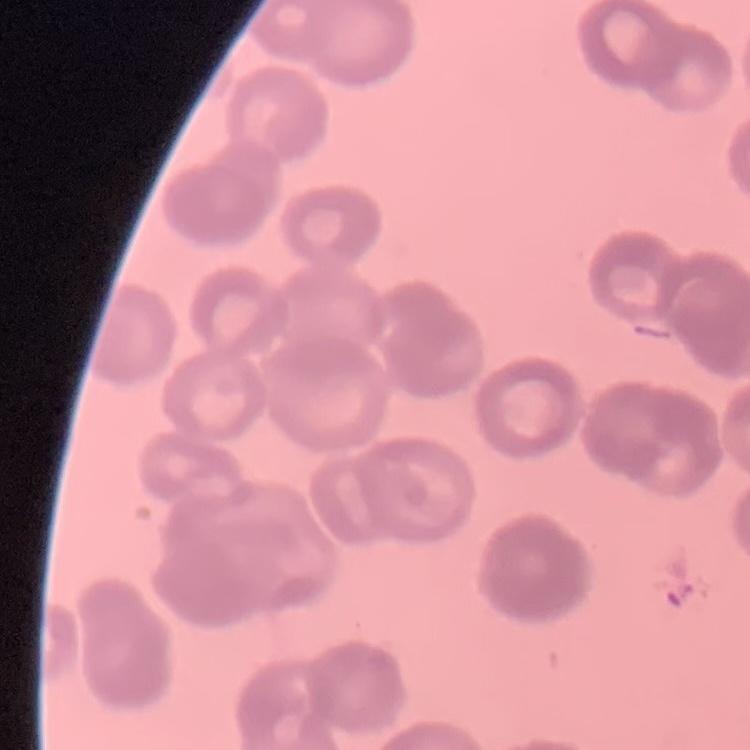

Summary:
  - Erythrocyte morphology: rouleaux formation
  - Preparation: thin blood smear
  - Stain: Field's or Giemsa
  - Image type: square crop of a larger photomicrograph